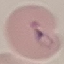

Malaria status: parasitized. Photographed with a smartphone camera at the microscope eyepiece. Cell patch, automatically extracted from a larger field of view and resized to 64 × 64 pixels. Thin smear of blood. Giemsa-stained preparation.